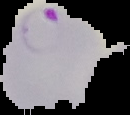
Result: malaria parasites detected. From a thin blood smear. Image is 130×115 pixels. Cell region segmented out of the field of view; the surrounding area is masked to black.